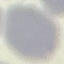

Summary:
  - Result: no malaria parasites seen
  - Stain: Giemsa
  - Preparation: thin smear
  - Capture: smartphone through the microscope eyepiece
  - Image type: automatically extracted cell patch, resized to 64 × 64 pixels